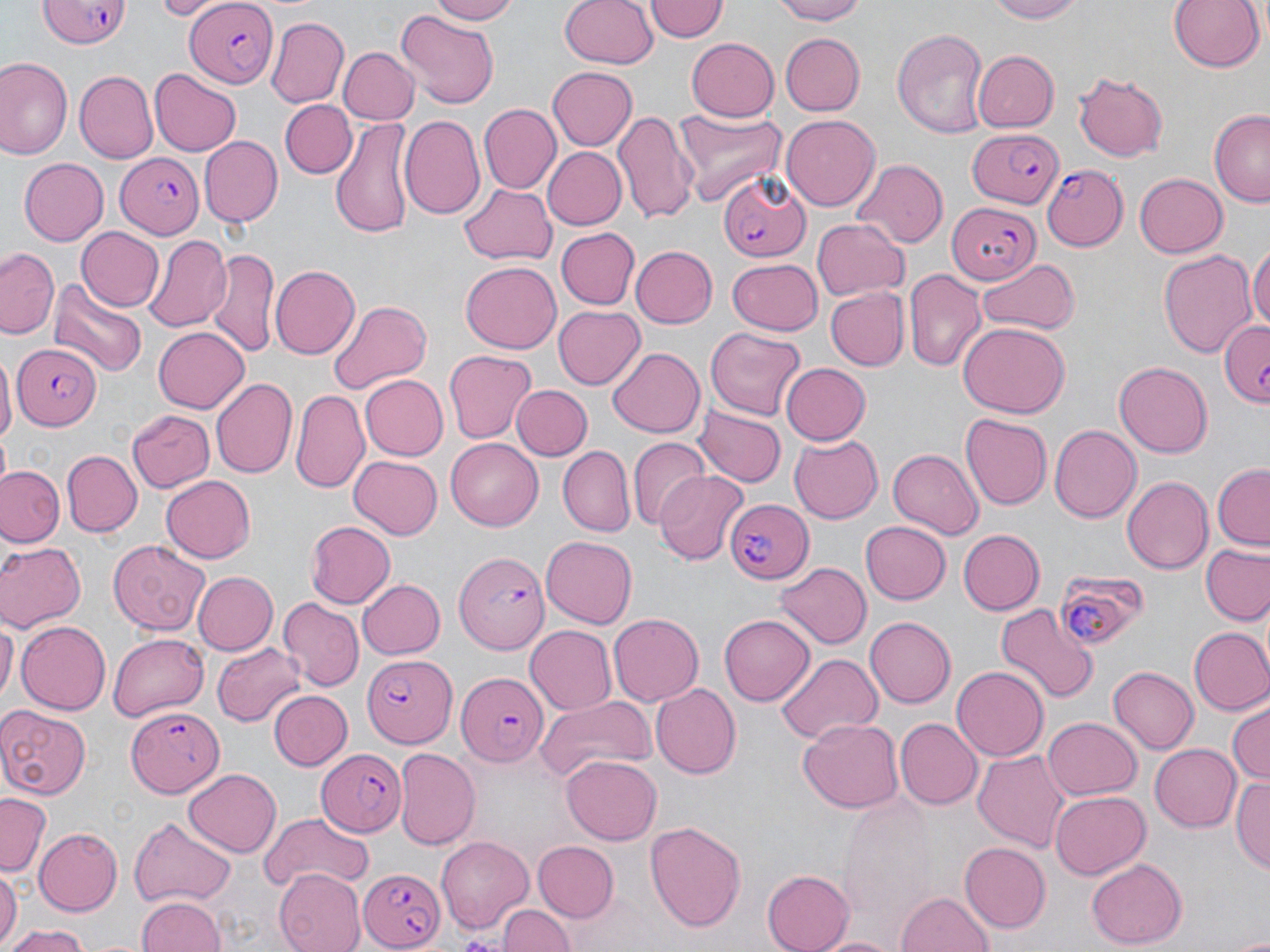
slide-level diagnosis = Plasmodium falciparum
field of view = one of a larger specimen
Plasmodium falciparum-infected red blood cell locations = approximate bounding boxes as named x1/y1/x2/y2 corners in pixels: (x1=39, y1=0, x2=131, y2=52), (x1=182, y1=1, x2=276, y2=87), (x1=964, y1=124, x2=1068, y2=211), (x1=116, y1=153, x2=204, y2=238), (x1=1040, y1=164, x2=1127, y2=250), (x1=717, y1=169, x2=813, y2=265), (x1=944, y1=199, x2=1042, y2=285), (x1=1216, y1=319, x2=1268, y2=409), (x1=12, y1=344, x2=99, y2=430), (x1=727, y1=496, x2=814, y2=585), (x1=452, y1=551, x2=551, y2=653), (x1=1056, y1=572, x2=1153, y2=646), (x1=354, y1=648, x2=456, y2=753), (x1=457, y1=673, x2=546, y2=764), (x1=126, y1=706, x2=226, y2=799), (x1=318, y1=747, x2=407, y2=839), (x1=357, y1=863, x2=447, y2=951)
stain = May-Grünwald-Giemsa
image size = 1270×952 pixels
uninfected red blood cell locations = approximate bounding boxes as named x1/y1/x2/y2 corners in pixels: (x1=155, y1=0, x2=214, y2=18), (x1=425, y1=0, x2=518, y2=24), (x1=559, y1=0, x2=660, y2=70), (x1=769, y1=0, x2=870, y2=24), (x1=986, y1=0, x2=1087, y2=23), (x1=1168, y1=0, x2=1262, y2=74), (x1=645, y1=1, x2=727, y2=43), (x1=398, y1=12, x2=499, y2=111), (x1=266, y1=15, x2=350, y2=106), (x1=893, y1=27, x2=990, y2=138), (x1=778, y1=33, x2=865, y2=116), (x1=684, y1=38, x2=779, y2=121), (x1=336, y1=47, x2=417, y2=124), (x1=971, y1=49, x2=1058, y2=131), (x1=0, y1=57, x2=70, y2=159), (x1=548, y1=66, x2=636, y2=149), (x1=149, y1=70, x2=241, y2=156), (x1=1071, y1=71, x2=1169, y2=163), (x1=74, y1=73, x2=158, y2=166), (x1=280, y1=100, x2=358, y2=178), (x1=480, y1=104, x2=559, y2=193), (x1=673, y1=108, x2=787, y2=206), (x1=612, y1=110, x2=697, y2=226), (x1=1208, y1=110, x2=1269, y2=204), (x1=782, y1=114, x2=881, y2=209), (x1=399, y1=115, x2=486, y2=221), (x1=331, y1=117, x2=415, y2=242), (x1=201, y1=136, x2=282, y2=227), (x1=540, y1=147, x2=625, y2=230), (x1=19, y1=159, x2=109, y2=245), (x1=850, y1=160, x2=946, y2=249), (x1=1134, y1=172, x2=1227, y2=258), (x1=459, y1=183, x2=560, y2=265), (x1=813, y1=216, x2=910, y2=301), (x1=75, y1=226, x2=165, y2=312), (x1=555, y1=226, x2=637, y2=307), (x1=144, y1=235, x2=231, y2=333), (x1=1247, y1=244, x2=1270, y2=334), (x1=629, y1=245, x2=716, y2=329), (x1=2, y1=246, x2=61, y2=340), (x1=205, y1=248, x2=277, y2=359), (x1=1156, y1=248, x2=1257, y2=359), (x1=726, y1=258, x2=824, y2=334), (x1=977, y1=259, x2=1077, y2=334), (x1=460, y1=262, x2=561, y2=355), (x1=270, y1=264, x2=360, y2=360), (x1=904, y1=267, x2=986, y2=372), (x1=51, y1=278, x2=147, y2=379), (x1=824, y1=287, x2=909, y2=372), (x1=325, y1=298, x2=434, y2=399), (x1=552, y1=304, x2=645, y2=391), (x1=955, y1=322, x2=1071, y2=418), (x1=154, y1=325, x2=250, y2=412), (x1=703, y1=328, x2=807, y2=421), (x1=609, y1=347, x2=705, y2=438), (x1=444, y1=351, x2=535, y2=443), (x1=0, y1=352, x2=16, y2=448), (x1=778, y1=361, x2=869, y2=445), (x1=1114, y1=362, x2=1214, y2=457), (x1=360, y1=374, x2=448, y2=461), (x1=212, y1=376, x2=297, y2=478), (x1=510, y1=385, x2=591, y2=460), (x1=291, y1=391, x2=369, y2=494), (x1=126, y1=407, x2=215, y2=492), (x1=695, y1=407, x2=785, y2=487), (x1=960, y1=414, x2=1050, y2=509), (x1=1049, y1=423, x2=1142, y2=522), (x1=790, y1=433, x2=883, y2=522), (x1=445, y1=437, x2=542, y2=531), (x1=630, y1=441, x2=709, y2=527), (x1=556, y1=446, x2=634, y2=535), (x1=886, y1=449, x2=984, y2=539), (x1=63, y1=451, x2=141, y2=535), (x1=349, y1=453, x2=444, y2=539), (x1=0, y1=464, x2=64, y2=546), (x1=1211, y1=464, x2=1269, y2=549), (x1=656, y1=469, x2=748, y2=563), (x1=161, y1=476, x2=256, y2=563), (x1=1122, y1=476, x2=1212, y2=572), (x1=858, y1=519, x2=949, y2=605), (x1=304, y1=521, x2=394, y2=609), (x1=958, y1=529, x2=1045, y2=615), (x1=540, y1=535, x2=636, y2=629), (x1=106, y1=539, x2=210, y2=638), (x1=0, y1=541, x2=83, y2=632), (x1=1200, y1=544, x2=1270, y2=625), (x1=774, y1=562, x2=871, y2=650), (x1=191, y1=571, x2=277, y2=655), (x1=357, y1=578, x2=445, y2=660), (x1=279, y1=598, x2=363, y2=689), (x1=994, y1=602, x2=1098, y2=707), (x1=608, y1=613, x2=705, y2=706), (x1=721, y1=614, x2=814, y2=706), (x1=0, y1=616, x2=16, y2=711), (x1=865, y1=616, x2=956, y2=709), (x1=13, y1=621, x2=110, y2=714), (x1=525, y1=624, x2=617, y2=714), (x1=1189, y1=627, x2=1270, y2=715), (x1=107, y1=632, x2=208, y2=720), (x1=210, y1=642, x2=305, y2=727), (x1=775, y1=653, x2=883, y2=746), (x1=951, y1=667, x2=1047, y2=758), (x1=1107, y1=667, x2=1198, y2=755), (x1=649, y1=682, x2=742, y2=779), (x1=268, y1=690, x2=352, y2=771), (x1=535, y1=694, x2=657, y2=782), (x1=1227, y1=702, x2=1269, y2=785), (x1=0, y1=705, x2=91, y2=800), (x1=799, y1=717, x2=905, y2=813), (x1=1043, y1=717, x2=1142, y2=801), (x1=896, y1=718, x2=982, y2=809), (x1=1150, y1=743, x2=1242, y2=831), (x1=393, y1=747, x2=480, y2=851), (x1=973, y1=749, x2=1072, y2=854), (x1=561, y1=755, x2=660, y2=844), (x1=184, y1=766, x2=280, y2=855), (x1=1230, y1=777, x2=1270, y2=871), (x1=1050, y1=791, x2=1149, y2=880), (x1=0, y1=794, x2=49, y2=879), (x1=260, y1=810, x2=373, y2=894), (x1=129, y1=817, x2=236, y2=906), (x1=644, y1=821, x2=748, y2=932), (x1=35, y1=828, x2=122, y2=913), (x1=436, y1=837, x2=533, y2=931), (x1=961, y1=841, x2=1050, y2=931), (x1=534, y1=842, x2=619, y2=921), (x1=1085, y1=858, x2=1185, y2=948), (x1=0, y1=867, x2=21, y2=949), (x1=274, y1=868, x2=365, y2=952), (x1=763, y1=868, x2=857, y2=952), (x1=5, y1=884, x2=44, y2=945), (x1=898, y1=893, x2=994, y2=952), (x1=135, y1=896, x2=225, y2=952), (x1=497, y1=901, x2=572, y2=952), (x1=5, y1=924, x2=88, y2=952), (x1=819, y1=933, x2=896, y2=952)
magnification = 1000x
preparation = thin blood smear
modality = optical microscopy